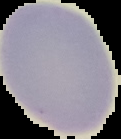

image_size: 121×139 pixels
result: no Plasmodium parasites detected
preparation: thin blood film
image_type: segmented cell region on a black background